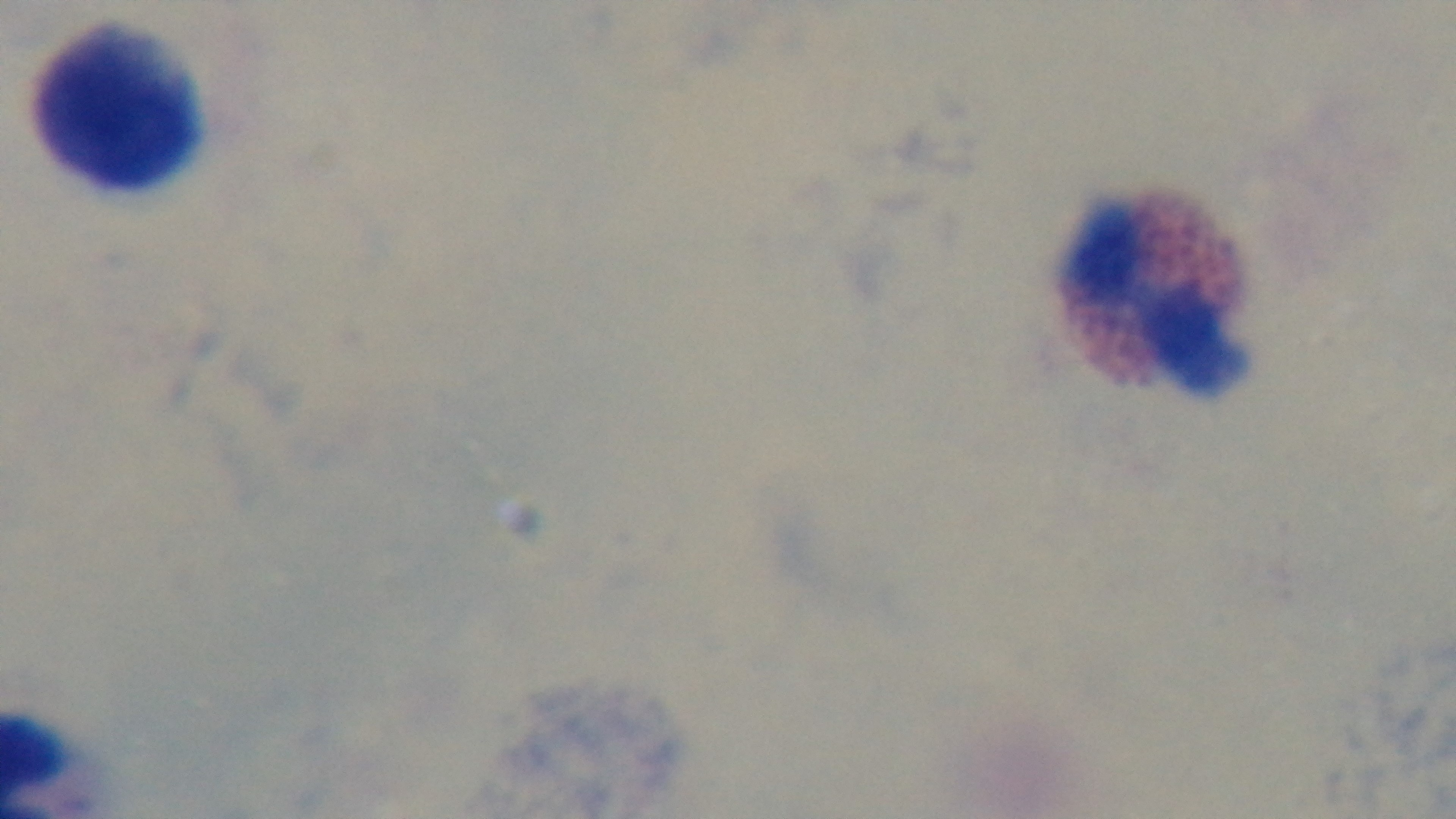

{
  "preparation": "thick blood film",
  "field_of_view": "one from the slide",
  "modality": "light microscopy",
  "objective": "100x oil immersion",
  "capture": "mounted 4K digital camera",
  "stain": "Giemsa",
  "malaria_status": "negative"
}